Assess for malaria.
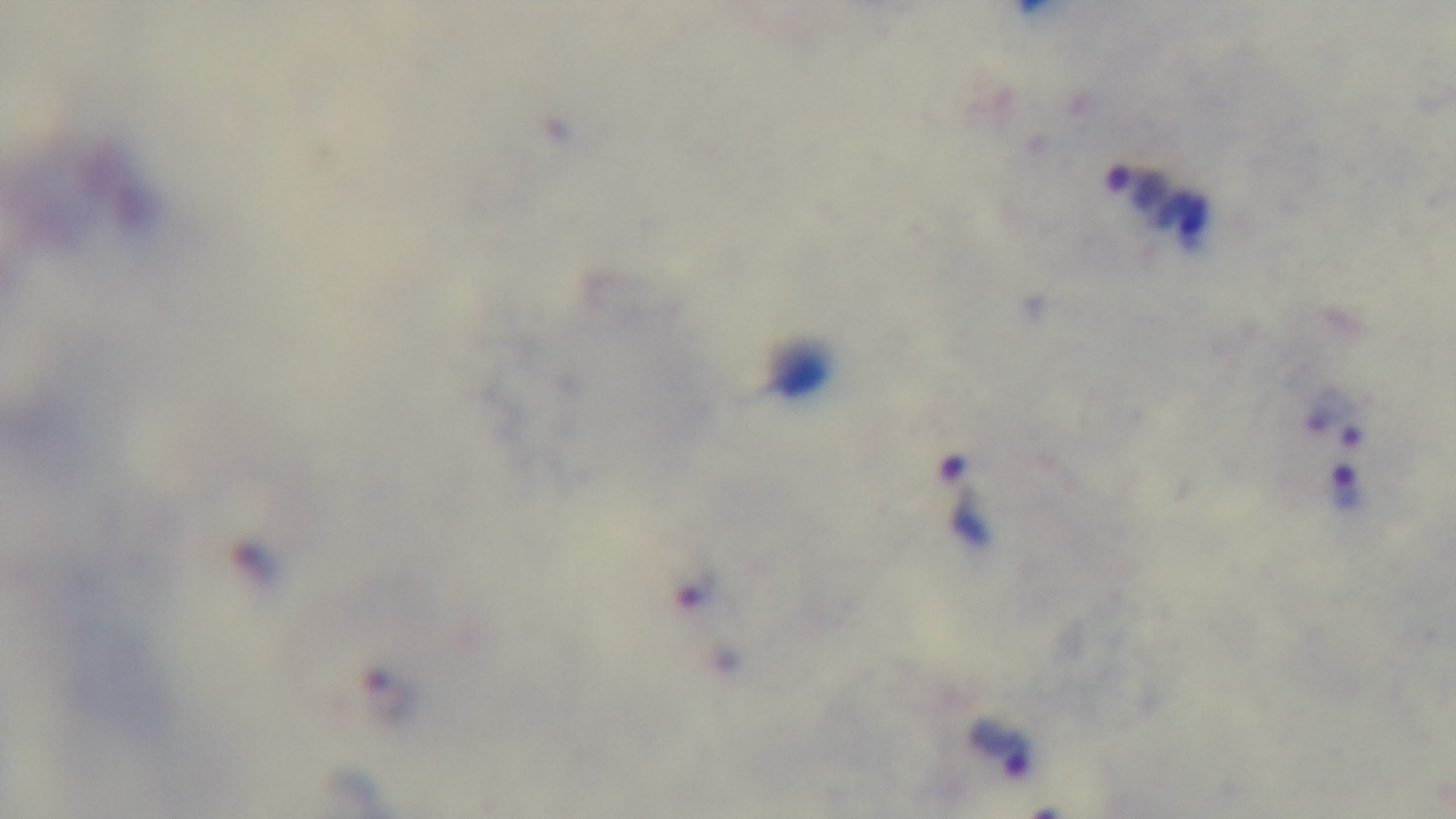

Infected.

Giemsa stain. Light microscopy. Oil-immersion objective, 100x. One field from the slide. Preparation: thick smear. Captured with a mounted 4K digital camera.